Identify the parasite.
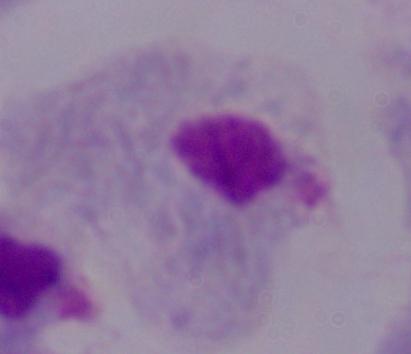

A trichomonad.

magnification = 1000x
modality = micrograph